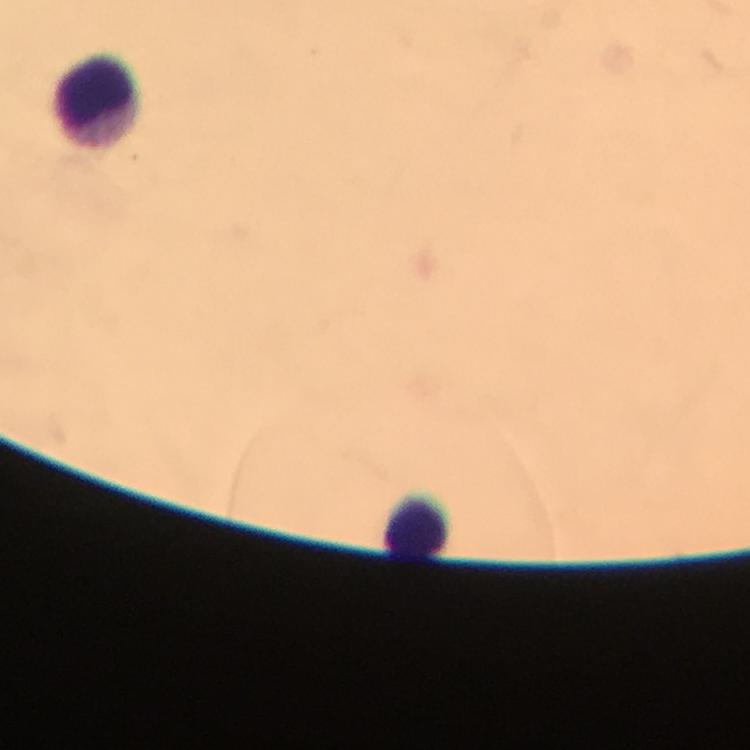

Approximate centers as {x, y} in pixels. Leukocyte locations: {101, 101}, {418, 523}. Malaria parasites: none seen. Giemsa stain. Photographed with a smartphone mounted on the microscope. Cropped region of a single field of view. From a diagnostic examination for malaria. Immersion oil applied. Thick blood smear. 100x magnification. Image is 750×750 pixels.